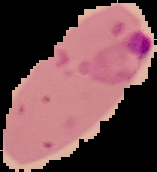
image type = segmented cell region on a black background
preparation = thin blood film
image size = 157×172 pixels
result = Plasmodium parasites identified